Locate every blood parasite and identify its species.
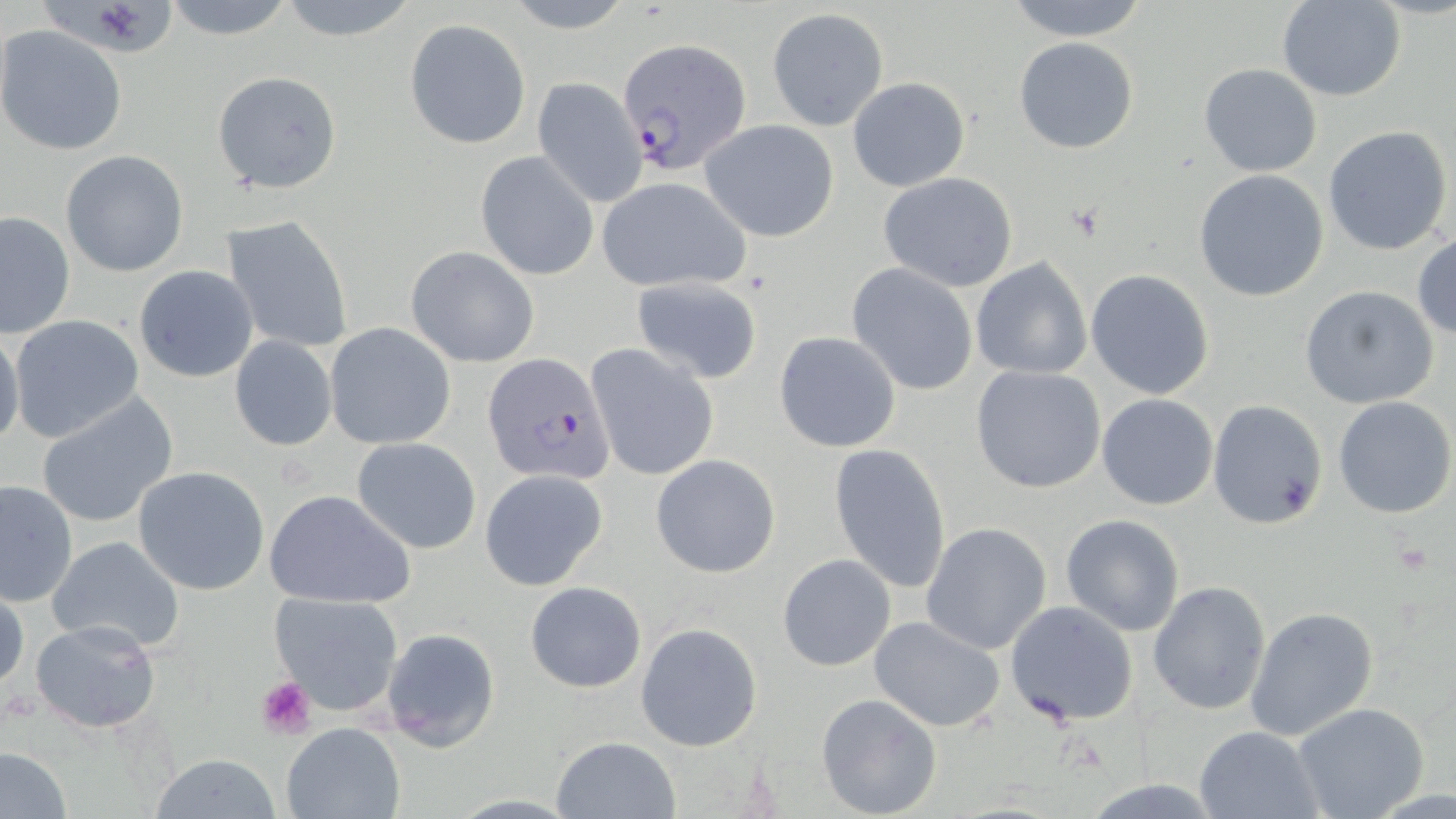
Approximate bounding boxes as named x1/y1/x2/y2 corners in pixels.
Plasmodium falciparum-infected red blood cells: (x1=615, y1=37, x2=752, y2=176), (x1=484, y1=354, x2=615, y2=485).
No Plasmodium ovale, Plasmodium malariae, Plasmodium vivax, Babesia divergens, or Trypanosoma brucei observed.

Summary:
  - Uninfected red blood cell locations: (x1=35, y1=0, x2=181, y2=60), (x1=159, y1=0, x2=298, y2=41), (x1=274, y1=0, x2=420, y2=42), (x1=1000, y1=0, x2=1152, y2=40), (x1=1276, y1=0, x2=1404, y2=100), (x1=498, y1=1, x2=639, y2=33), (x1=767, y1=8, x2=887, y2=130), (x1=404, y1=19, x2=531, y2=149), (x1=1, y1=25, x2=128, y2=156), (x1=1014, y1=37, x2=1138, y2=154), (x1=1198, y1=62, x2=1322, y2=176), (x1=214, y1=70, x2=342, y2=193), (x1=847, y1=77, x2=969, y2=192), (x1=532, y1=78, x2=648, y2=207), (x1=699, y1=119, x2=842, y2=241), (x1=1322, y1=124, x2=1453, y2=256), (x1=61, y1=150, x2=189, y2=277), (x1=476, y1=151, x2=598, y2=280), (x1=1194, y1=168, x2=1329, y2=302), (x1=879, y1=172, x2=1018, y2=292), (x1=594, y1=175, x2=752, y2=294), (x1=0, y1=212, x2=75, y2=339), (x1=221, y1=215, x2=355, y2=353), (x1=1412, y1=232, x2=1456, y2=340), (x1=406, y1=246, x2=540, y2=367), (x1=970, y1=258, x2=1093, y2=379), (x1=846, y1=262, x2=980, y2=396), (x1=134, y1=266, x2=258, y2=382), (x1=1086, y1=269, x2=1215, y2=398), (x1=631, y1=276, x2=762, y2=383), (x1=1300, y1=285, x2=1439, y2=410), (x1=7, y1=314, x2=145, y2=442), (x1=324, y1=323, x2=455, y2=450), (x1=0, y1=327, x2=24, y2=451), (x1=774, y1=332, x2=901, y2=453), (x1=228, y1=335, x2=339, y2=452), (x1=586, y1=344, x2=719, y2=483), (x1=971, y1=365, x2=1107, y2=494), (x1=36, y1=393, x2=179, y2=529), (x1=1097, y1=394, x2=1218, y2=510), (x1=1332, y1=395, x2=1456, y2=520), (x1=1209, y1=400, x2=1327, y2=527), (x1=352, y1=436, x2=482, y2=555), (x1=829, y1=442, x2=951, y2=594), (x1=651, y1=455, x2=779, y2=576), (x1=133, y1=465, x2=273, y2=596), (x1=480, y1=468, x2=610, y2=593), (x1=0, y1=477, x2=78, y2=608), (x1=264, y1=488, x2=416, y2=609), (x1=1060, y1=514, x2=1185, y2=637), (x1=925, y1=518, x2=1187, y2=644), (x1=920, y1=521, x2=1053, y2=655), (x1=45, y1=535, x2=188, y2=655), (x1=777, y1=554, x2=896, y2=672), (x1=524, y1=580, x2=647, y2=693), (x1=1148, y1=581, x2=1271, y2=717), (x1=1, y1=584, x2=27, y2=696), (x1=268, y1=591, x2=405, y2=716), (x1=1005, y1=600, x2=1138, y2=726), (x1=1246, y1=605, x2=1378, y2=742), (x1=869, y1=615, x2=1006, y2=732), (x1=29, y1=619, x2=162, y2=734), (x1=635, y1=623, x2=763, y2=751), (x1=381, y1=627, x2=500, y2=752), (x1=815, y1=692, x2=941, y2=819), (x1=1294, y1=703, x2=1429, y2=819), (x1=280, y1=724, x2=404, y2=819), (x1=1194, y1=726, x2=1322, y2=818), (x1=551, y1=736, x2=681, y2=819), (x1=0, y1=747, x2=71, y2=817), (x1=147, y1=754, x2=284, y2=818), (x1=1080, y1=778, x2=1226, y2=816)
  - Platelet locations: (x1=255, y1=676, x2=318, y2=742)
  - Slide-level diagnosis: Plasmodium falciparum
  - Modality: light microscopy
  - Image size: 1456×819 pixels
  - Magnification: 1000x
  - Stain: May-Grünwald-Giemsa
  - Preparation: thin blood smear
  - Field of view: one of a larger specimen